State which parasite is depicted.
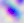
Toxoplasma gondii.

modality = photomicrograph
magnification = 400x